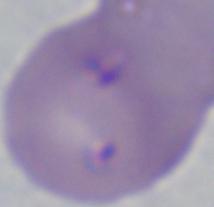
Summary:
  - Modality: micrograph
  - Identification: Babesia
  - Magnification: 1000x